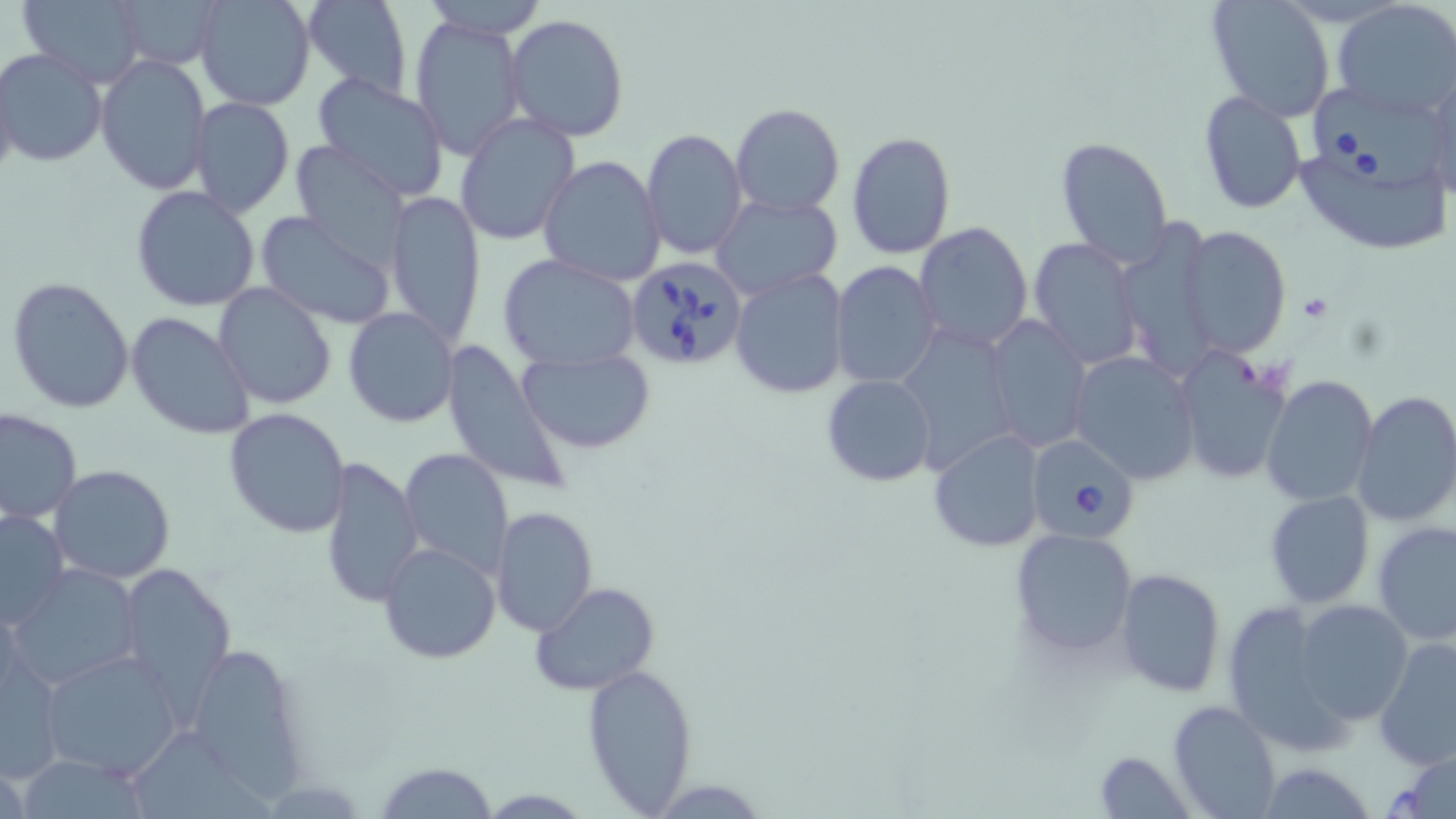 Approximate bounding boxes as (x1,y1)-(x2,y2) corner pairs in pixels. Uninfected red blood cell locations: (16,0)-(149,88), (111,0)-(224,69), (194,0)-(314,111), (301,0)-(411,98), (420,0)-(550,40), (1205,0)-(1337,124), (1332,1)-(1456,117), (409,14)-(526,161), (506,14)-(630,142), (0,47)-(106,167), (95,56)-(211,194), (1,63)-(19,192), (1427,65)-(1456,200), (313,73)-(449,199), (1198,91)-(1307,214), (189,97)-(293,217), (731,103)-(844,217), (454,113)-(579,245), (642,129)-(749,259), (846,131)-(956,260), (1297,133)-(1452,257), (1055,137)-(1173,266), (290,144)-(412,268), (539,156)-(667,287), (131,186)-(260,313), (386,191)-(485,347), (712,194)-(842,298), (253,209)-(396,331), (913,220)-(1033,353), (1125,221)-(1215,382), (1176,226)-(1292,358), (1029,237)-(1143,370), (498,253)-(640,372), (831,260)-(942,388), (729,267)-(849,399), (6,276)-(134,414), (214,283)-(339,410), (344,308)-(460,428), (127,312)-(255,441), (984,314)-(1094,452), (443,343)-(571,495), (517,346)-(657,454), (1170,349)-(1290,485), (1069,350)-(1202,484), (821,375)-(936,487), (1260,375)-(1379,506), (1353,390)-(1456,526), (0,407)-(82,523), (223,408)-(350,540), (928,429)-(1045,553), (396,447)-(513,579), (319,453)-(425,608), (48,465)-(176,584), (1264,491)-(1374,608), (489,506)-(599,636), (0,509)-(70,629), (1373,520)-(1456,645), (1011,527)-(1140,657), (377,542)-(500,665), (8,563)-(143,692), (118,564)-(237,715), (1115,568)-(1225,698), (531,582)-(659,697), (1291,599)-(1414,726), (1222,600)-(1350,748), (180,635)-(311,800), (1375,636)-(1456,772), (38,647)-(185,781), (1,651)-(69,782), (582,663)-(699,813), (1168,700)-(1280,819), (126,729)-(282,819), (1381,748)-(1456,818), (1094,750)-(1199,819), (1255,761)-(1379,817), (374,762)-(498,817). Platelet locations: (1299,293)-(1333,322). Babesia divergens-infected red blood cell locations: (1307,85)-(1449,192), (625,257)-(749,372), (1025,434)-(1141,545). Slide-level diagnosis: Babesia divergens. Single field of view. Image is 1456×819 pixels. 1000x magnification. Thin blood smear. May-Grünwald-Giemsa-stained preparation. Optical microscopy.